Locate every blood parasite and identify its species.
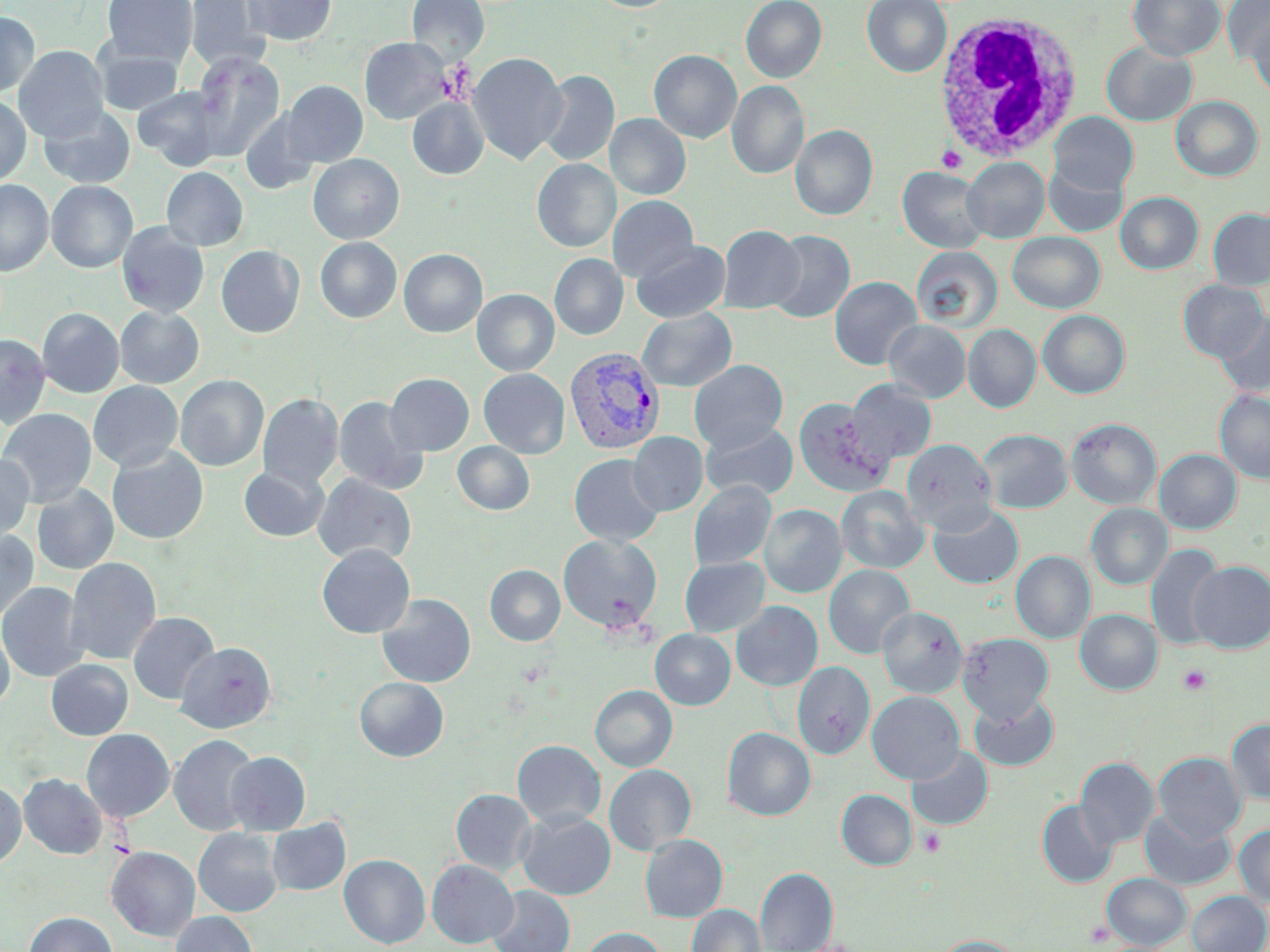
Approximate bounding boxes as (x1, y1, x2, y2) in pixels.
Plasmodium vivax-infected red blood cells: (564, 346, 665, 455).
No Plasmodium falciparum, Plasmodium ovale, Plasmodium malariae, Babesia divergens, or Trypanosoma brucei observed.

slide_level_diagnosis: Plasmodium vivax
white_blood_cell_locations: 'approximate bounding boxes as (x1, y1, x2, y2) in pixels: (933, 11, 1083, 163)'
modality: optical microscopy
image_size: 1270×952 pixels
magnification: 1000x
platelet_locations: 'approximate bounding boxes as (x1, y1, x2, y2) in pixels: (440, 59, 475, 103), (936, 145, 966, 173), (518, 659, 549, 688), (1178, 665, 1211, 694), (919, 828, 946, 856), (1086, 919, 1112, 946)'
preparation: thin blood smear
uninfected_red_blood_cell_locations: 'approximate bounding boxes as (x1, y1, x2, y2) in pixels: (101, 0, 198, 65), (186, 0, 270, 72), (242, 0, 338, 45), (407, 0, 489, 64), (589, 0, 680, 12), (740, 0, 827, 83), (862, 0, 952, 77), (1128, 0, 1226, 62), (1222, 1, 1270, 64), (0, 12, 39, 98), (1248, 15, 1270, 100), (360, 37, 452, 124), (1101, 42, 1197, 126), (13, 45, 109, 142), (93, 45, 184, 115), (649, 50, 742, 143), (191, 52, 285, 159), (468, 52, 568, 165), (537, 69, 619, 167), (727, 80, 809, 180), (279, 81, 368, 166), (132, 86, 227, 170), (0, 95, 31, 186), (1171, 96, 1263, 181), (407, 97, 489, 180), (38, 106, 136, 189), (239, 109, 323, 195), (1049, 112, 1138, 196), (604, 114, 691, 199), (790, 124, 877, 221), (308, 154, 404, 244), (961, 157, 1050, 243), (532, 158, 621, 252), (1044, 160, 1129, 237), (161, 167, 248, 251), (898, 167, 991, 254), (0, 180, 53, 276), (46, 180, 138, 272), (1115, 192, 1203, 275), (607, 195, 698, 283), (1208, 208, 1270, 291), (117, 222, 209, 318), (717, 225, 805, 314), (766, 230, 855, 323), (1007, 232, 1106, 313), (315, 237, 402, 323), (631, 239, 731, 323), (216, 245, 305, 338), (911, 245, 1002, 333), (398, 248, 488, 337), (549, 254, 628, 340), (828, 276, 923, 370), (1178, 280, 1268, 362), (472, 289, 559, 376), (114, 306, 204, 388), (37, 307, 124, 398), (637, 308, 737, 392), (1037, 310, 1130, 398), (1215, 312, 1270, 398), (884, 320, 971, 403), (963, 324, 1041, 413), (0, 333, 50, 429), (689, 359, 788, 453), (478, 368, 570, 458), (385, 373, 474, 455), (175, 374, 269, 472), (845, 378, 937, 465), (88, 381, 183, 472), (1215, 389, 1270, 485), (257, 393, 343, 490), (333, 395, 428, 495), (793, 397, 891, 496), (0, 408, 96, 507), (1066, 418, 1162, 509), (700, 420, 799, 502), (978, 429, 1072, 513), (628, 431, 708, 516), (901, 438, 997, 534), (452, 441, 535, 515), (106, 445, 209, 545), (1155, 449, 1242, 534), (0, 453, 34, 542), (568, 453, 665, 546), (238, 465, 329, 542), (312, 473, 417, 567), (688, 480, 776, 570), (32, 484, 118, 574), (836, 485, 929, 574), (928, 503, 1024, 590), (1086, 503, 1173, 589), (760, 504, 846, 598), (0, 528, 39, 624), (557, 533, 663, 633), (1145, 543, 1225, 650), (316, 544, 415, 638), (1010, 551, 1096, 643), (65, 556, 162, 666), (679, 556, 770, 637), (1189, 560, 1270, 652), (485, 565, 565, 646), (823, 565, 915, 659), (0, 582, 89, 682), (376, 593, 476, 688), (731, 601, 823, 691), (877, 606, 968, 698), (1075, 609, 1163, 695), (128, 611, 219, 705), (0, 620, 15, 710), (650, 629, 735, 710), (958, 632, 1053, 721), (175, 642, 277, 733), (45, 659, 133, 740), (792, 662, 875, 759), (354, 677, 448, 762), (590, 685, 677, 771), (867, 692, 964, 784), (969, 695, 1059, 771), (1226, 718, 1270, 805), (722, 727, 815, 821), (81, 728, 175, 822), (168, 734, 259, 836), (512, 740, 606, 828), (906, 745, 993, 832), (226, 751, 311, 836), (1153, 752, 1246, 842), (1075, 757, 1160, 848), (604, 764, 696, 855), (19, 774, 107, 859), (0, 780, 26, 869), (451, 789, 537, 876), (836, 789, 917, 870), (1037, 800, 1118, 887), (1139, 809, 1236, 891), (516, 810, 616, 900), (267, 818, 351, 895), (1233, 825, 1270, 906), (193, 828, 283, 917), (640, 834, 727, 922), (107, 846, 200, 942), (339, 854, 430, 949), (426, 859, 518, 948), (756, 867, 838, 952), (1102, 873, 1191, 950), (487, 886, 575, 952), (1186, 891, 1270, 952), (686, 904, 766, 952), (170, 911, 258, 952), (24, 912, 117, 952), (578, 927, 669, 952), (935, 935, 1023, 952)'
field_of_view: single
stain: May-Grünwald-Giemsa